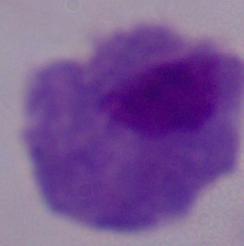

identification: trichomonad
magnification: 1000x
modality: photomicrograph